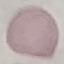

Result: no malaria parasites seen. Photographed with a smartphone camera at the microscope eyepiece. Thin blood smear. Automatically extracted cell patch, resized to 64 × 64 pixels. Giemsa stain.